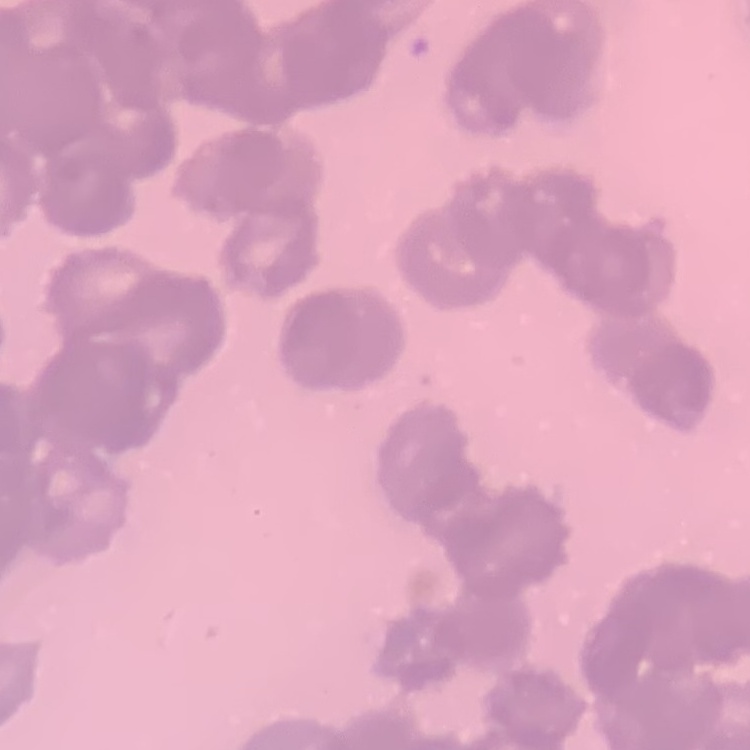
Summary:
  - Red blood cell morphology: rouleaux formation
  - Preparation: thin blood smear
  - Stain: Field's or Giemsa
  - Image type: square crop of a larger photomicrograph